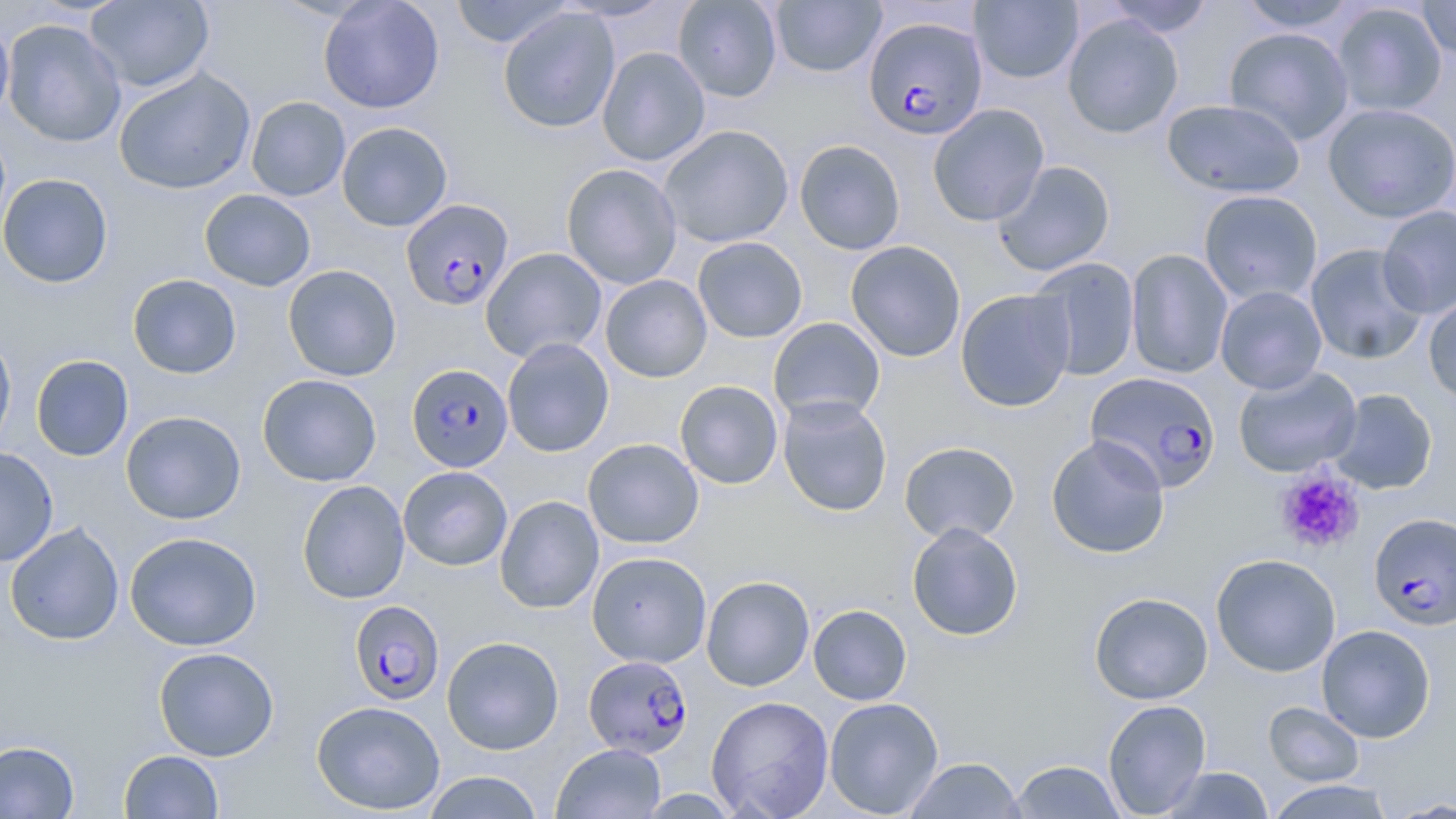

Approximate bounding boxes as (x1, y1, x2, y2) in pixels. Uninfected red blood cell locations: (85, 0, 213, 93), (318, 0, 444, 114), (448, 0, 574, 48), (555, 0, 675, 21), (673, 0, 782, 102), (770, 0, 886, 78), (970, 0, 1083, 84), (1103, 0, 1215, 37), (1236, 0, 1360, 34), (1417, 0, 1456, 61), (1332, 2, 1448, 117), (498, 7, 620, 133), (1062, 13, 1184, 139), (0, 15, 15, 126), (2, 18, 126, 147), (1223, 27, 1355, 145), (597, 46, 711, 166), (113, 67, 256, 195), (246, 96, 350, 201), (1162, 98, 1306, 199), (1324, 103, 1456, 223), (927, 104, 1050, 226), (336, 121, 453, 232), (658, 124, 794, 248), (794, 139, 905, 255), (992, 160, 1115, 276), (561, 163, 683, 289), (0, 173, 114, 288), (199, 189, 316, 291), (1198, 189, 1323, 306), (1377, 205, 1456, 319), (692, 236, 808, 343), (845, 241, 966, 362), (1305, 243, 1428, 364), (481, 247, 607, 363), (1125, 248, 1233, 379), (1027, 257, 1140, 381), (282, 264, 401, 381), (127, 274, 242, 379), (599, 274, 712, 383), (1215, 286, 1327, 394), (955, 288, 1076, 412), (1422, 294, 1456, 406), (768, 316, 885, 424), (0, 332, 16, 453), (501, 338, 614, 458), (30, 355, 133, 461), (1233, 366, 1362, 477), (257, 374, 382, 486), (675, 380, 783, 489), (1327, 388, 1438, 494), (777, 395, 893, 516), (121, 410, 246, 524), (1046, 434, 1170, 558), (582, 438, 704, 549), (899, 441, 1020, 545), (0, 447, 58, 567), (398, 466, 512, 570), (296, 480, 410, 604), (495, 495, 604, 614), (4, 521, 125, 646), (906, 522, 1024, 641), (124, 531, 262, 651), (587, 551, 712, 668), (1211, 553, 1341, 677), (701, 576, 814, 691), (1089, 592, 1213, 705), (808, 604, 912, 705), (1316, 625, 1436, 743), (441, 635, 564, 755), (153, 646, 279, 761), (706, 695, 834, 819), (824, 697, 944, 817), (1102, 699, 1212, 817), (311, 700, 446, 815), (1264, 702, 1364, 786), (0, 740, 80, 818), (552, 743, 665, 819), (119, 750, 224, 818), (903, 757, 1026, 818), (1009, 759, 1127, 818), (1158, 766, 1276, 818), (423, 771, 544, 818), (1264, 779, 1398, 819), (1386, 798, 1456, 818). Plasmodium falciparum-infected red blood cell locations: (868, 18, 992, 142), (400, 198, 514, 310), (407, 363, 513, 471), (1086, 371, 1222, 492), (1369, 513, 1456, 630), (351, 603, 445, 708), (583, 655, 693, 758). Platelet locations: (1275, 467, 1365, 554). Slide-level diagnosis: Plasmodium falciparum. Image is 1456×819 pixels. Light microscopy. Thin blood film. 1000x magnification. Single field of view. May-Grünwald-Giemsa-stained preparation.